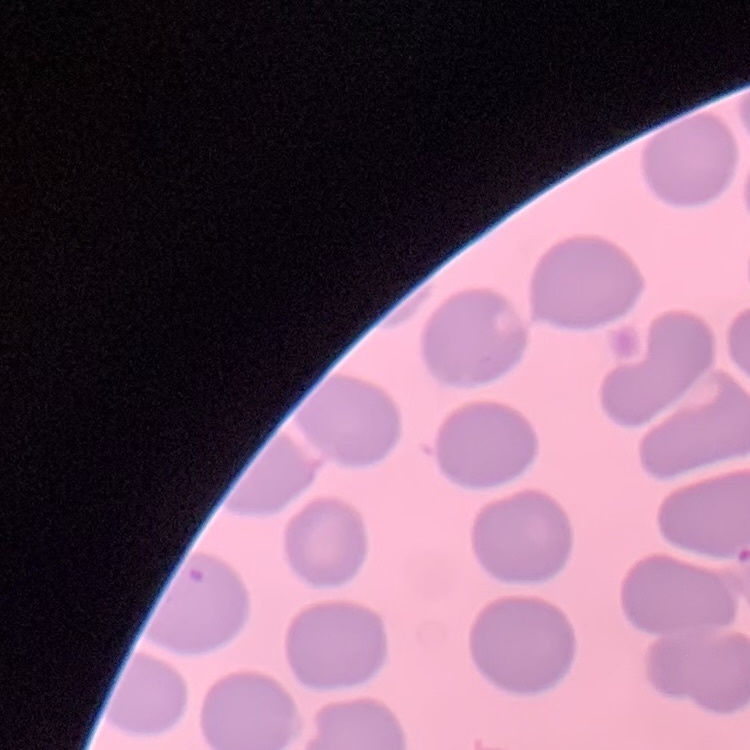 The erythrocytes exhibit no rouleaux formation. One tile cut from a larger photomicrograph. Thin blood film. Stained with either Field's or Giemsa.